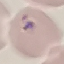

result = malaria parasites detected
stain = Giemsa
preparation = thin smear
image type = automatically extracted cell patch, resized to 64 × 64 pixels
capture = smartphone through the microscope eyepiece